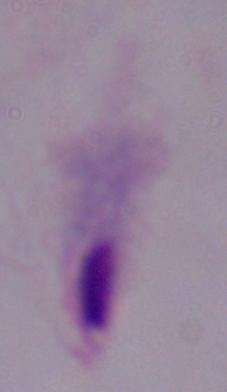 Captured at 1000x magnification. Micrograph. A trichomonad is shown.